Assess the morphology of the erythrocytes.
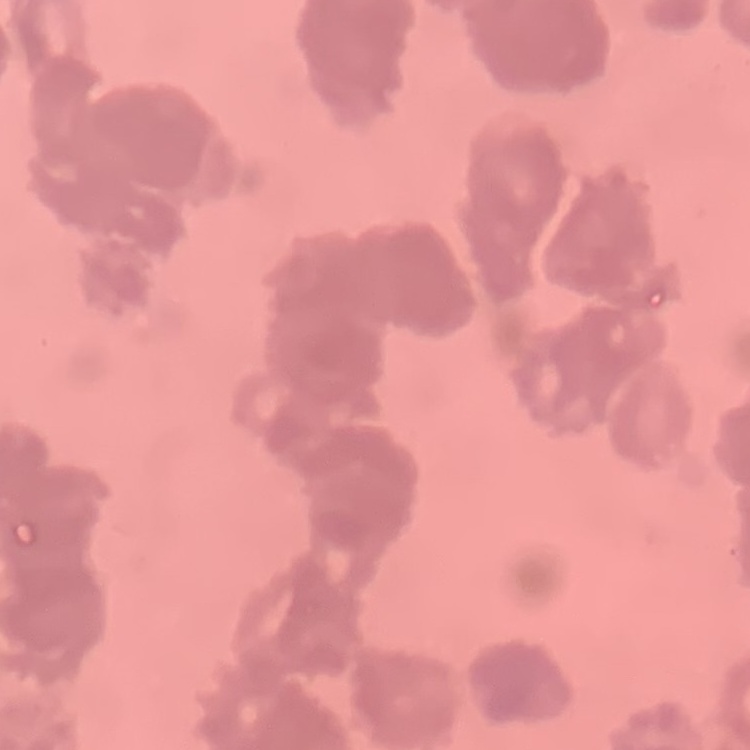

They show rouleaux formation.

Field's or Giemsa stain. One tile cut from a larger photomicrograph. Thin blood smear.